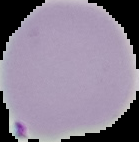
Segmented cell region on a black background. From a thin blood film. Image is 139×142 pixels. Result: Plasmodium parasites identified.